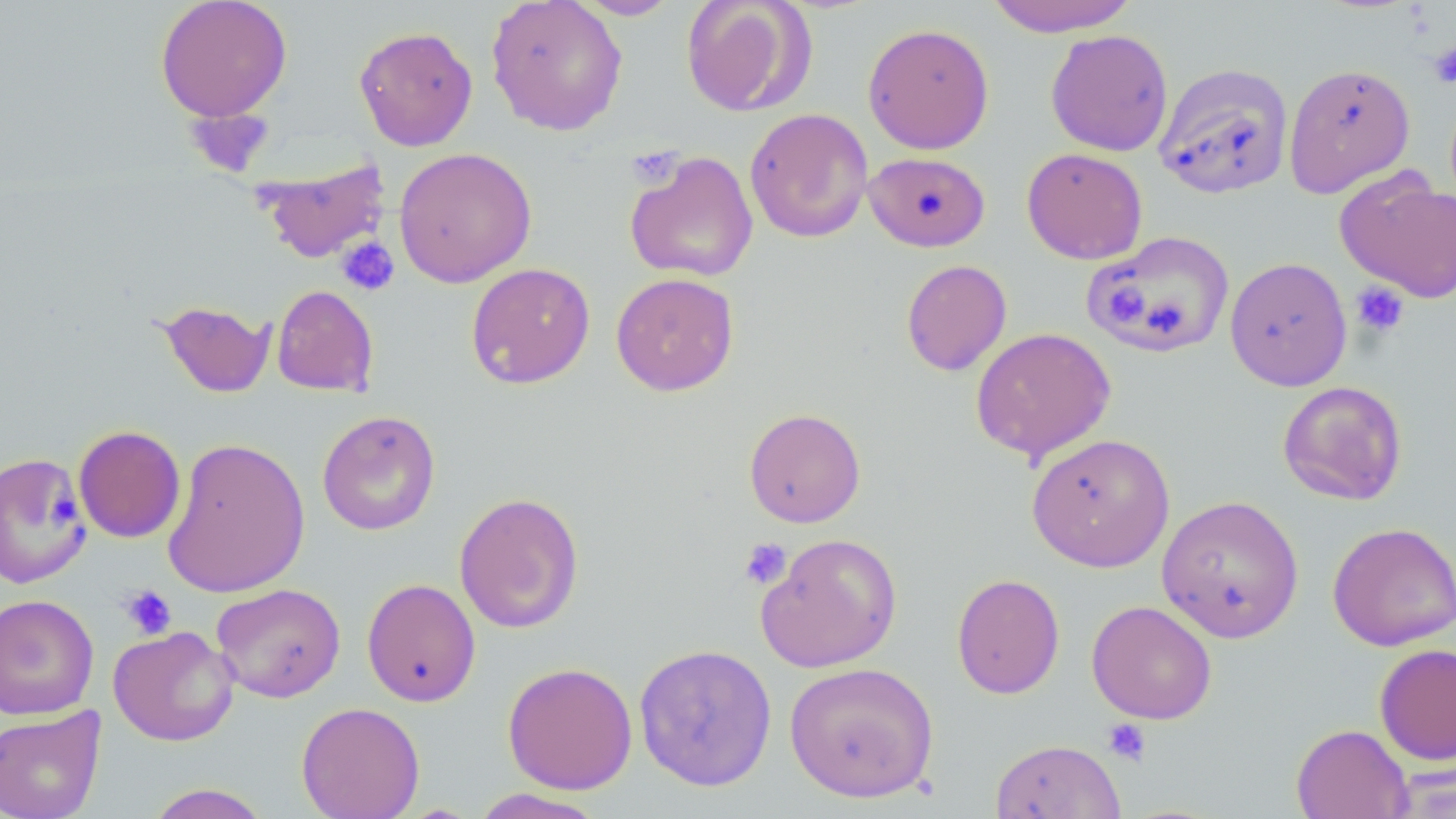
Summary:
  - Coordinate format: approximate bounding boxes as (x1,y1)-(x2,y2) corner pairs in pixels
  - Platelet locations: (1428,43)-(1456,87), (184,107)-(274,179), (626,144)-(684,190), (336,236)-(400,295), (1350,280)-(1410,339), (1110,287)-(1148,321), (738,537)-(793,590), (120,585)-(176,639), (1102,718)-(1152,767)
  - Uninfected red blood cell locations: (154,0)-(293,122), (485,0)-(629,137), (574,0)-(680,20), (681,0)-(814,117), (983,1)-(1140,37), (862,23)-(994,154), (353,25)-(478,151), (1045,29)-(1173,156), (1154,62)-(1294,200), (1284,62)-(1416,198), (744,107)-(873,243), (393,146)-(537,288), (1021,148)-(1148,264), (623,150)-(759,283), (864,151)-(990,252), (254,156)-(391,264), (1335,168)-(1456,303), (1082,230)-(1235,358), (1224,256)-(1353,391), (901,259)-(1012,376), (466,262)-(596,389), (610,273)-(739,396), (271,285)-(379,397), (157,299)-(274,398), (969,327)-(1117,464), (1277,380)-(1408,506), (743,407)-(866,527), (316,409)-(440,535), (73,425)-(186,543), (1026,432)-(1175,572), (162,436)-(311,598), (0,451)-(91,589), (454,491)-(585,634), (1156,494)-(1305,643), (1327,521)-(1456,651), (756,532)-(903,672), (951,573)-(1066,699), (361,578)-(481,707), (210,582)-(346,703), (0,593)-(99,720), (1086,600)-(1218,724), (108,625)-(240,746), (633,643)-(778,792), (1374,643)-(1456,767), (501,661)-(638,795), (784,661)-(939,803), (296,701)-(424,819), (0,706)-(106,819), (1290,723)-(1414,819), (989,738)-(1126,819), (1386,765)-(1456,818), (144,783)-(273,819), (470,788)-(609,818)
  - Slide-level diagnosis: negative for blood parasites
  - Preparation: thin blood film
  - Image size: 1456×819 pixels
  - Stain: May-Grünwald-Giemsa
  - Magnification: 1000x
  - Modality: optical microscopy
  - Field of view: one of a larger specimen